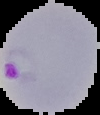
Summary:
  - Image size: 100×115 pixels
  - Image type: cell region segmented out of the field of view; surrounding area masked to black
  - Malaria status: parasitized
  - Preparation: thin blood smear